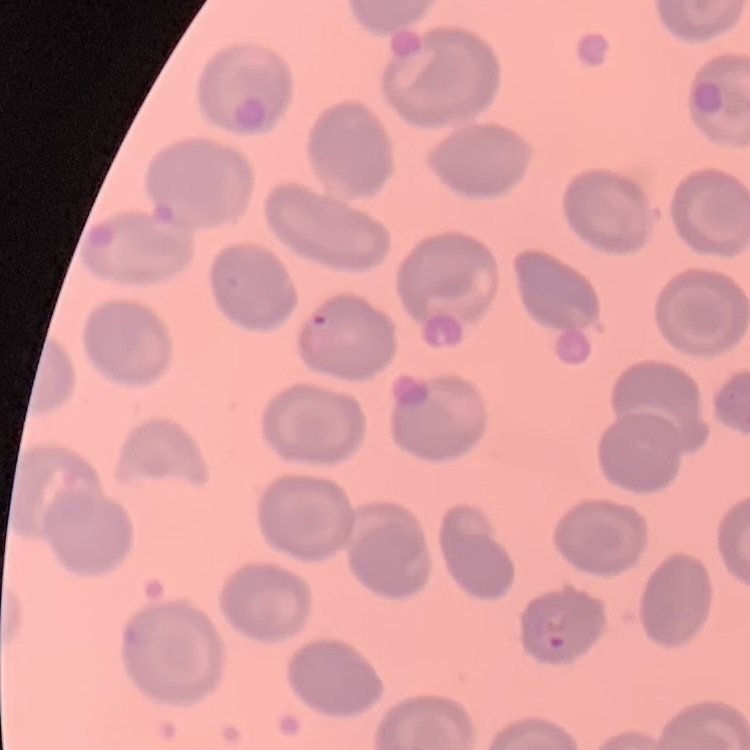
red_blood_cell_morphology: no rouleaux formation
preparation: thin peripheral smear
stain: Field's or Giemsa
image_type: square crop of a larger photomicrograph